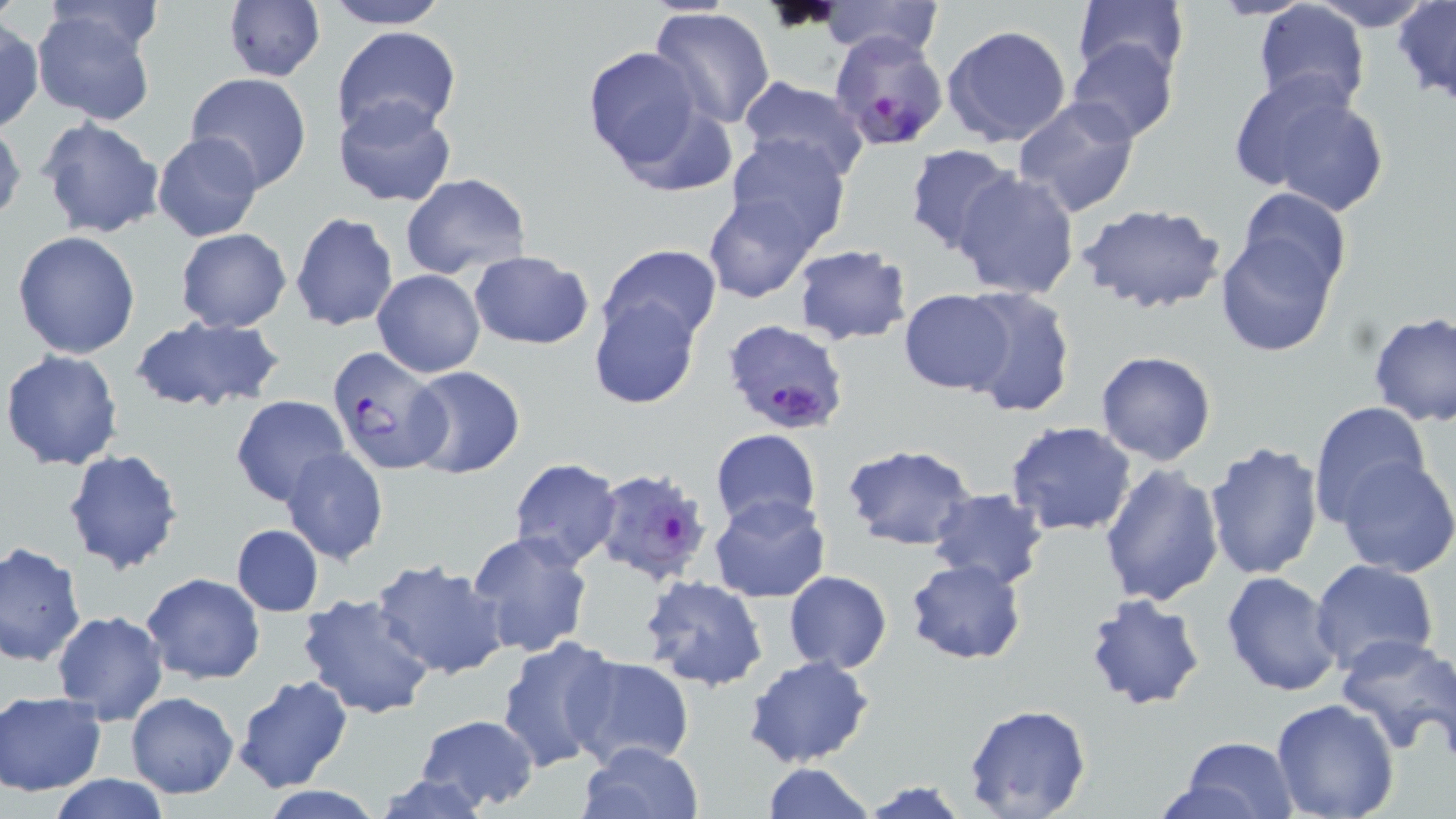
slide-level diagnosis = Plasmodium falciparum
field of view = single
uninfected red blood cell locations = approximate bounding boxes as [x1, y1, x2, y2] in pixels: [318, 0, 453, 28], [820, 0, 945, 62], [1073, 0, 1190, 86], [1310, 0, 1437, 29], [1393, 0, 1456, 107], [223, 2, 324, 83], [1252, 3, 1370, 117], [30, 5, 162, 126], [649, 7, 776, 129], [0, 19, 43, 134], [942, 24, 1073, 149], [331, 26, 461, 139], [1068, 38, 1179, 142], [580, 45, 715, 179], [184, 72, 313, 192], [1231, 73, 1393, 216], [735, 77, 872, 184], [331, 95, 458, 209], [1012, 95, 1141, 215], [36, 116, 164, 240], [0, 119, 25, 227], [152, 134, 264, 241], [723, 135, 849, 251], [903, 145, 1020, 258], [950, 168, 1082, 300], [400, 173, 530, 277], [1236, 186, 1351, 290], [704, 194, 820, 302], [1076, 203, 1227, 315], [289, 211, 400, 333], [175, 228, 292, 332], [11, 230, 142, 360], [1215, 231, 1340, 357], [790, 243, 914, 346], [600, 245, 721, 346], [466, 250, 594, 349], [373, 269, 485, 378], [959, 287, 1077, 417], [899, 289, 1017, 394], [587, 294, 701, 410], [1368, 312, 1456, 426], [127, 316, 287, 414], [2, 349, 124, 471], [1095, 350, 1216, 466], [404, 365, 526, 479], [231, 395, 352, 510], [1306, 400, 1433, 520], [1004, 420, 1138, 537], [710, 428, 821, 531], [1204, 440, 1324, 581], [841, 442, 979, 551], [281, 447, 388, 564], [62, 448, 183, 575], [1334, 456, 1456, 577], [508, 458, 623, 569], [1096, 463, 1224, 610], [927, 488, 1050, 590], [710, 495, 831, 604], [231, 523, 324, 617], [468, 531, 593, 657], [0, 543, 87, 667], [371, 558, 509, 680], [905, 558, 1027, 665], [1309, 560, 1441, 677], [1222, 570, 1345, 698], [783, 571, 892, 672], [141, 572, 267, 684], [640, 575, 770, 690], [298, 592, 438, 721], [1081, 593, 1206, 711], [51, 609, 169, 724], [1334, 632, 1456, 755], [495, 635, 621, 773], [1420, 645, 1455, 766], [563, 654, 695, 773], [743, 655, 876, 769], [233, 673, 353, 794], [1, 691, 105, 796], [125, 691, 240, 798], [1268, 698, 1401, 819], [963, 703, 1093, 819], [414, 712, 541, 811], [1170, 734, 1303, 818], [577, 740, 704, 819], [759, 762, 876, 819], [372, 767, 500, 819], [42, 776, 176, 818], [859, 777, 973, 819]
modality = optical microscopy
magnification = 1000x
stain = May-Grünwald-Giemsa
image size = 1456×819 pixels
Plasmodium falciparum-infected red blood cell locations = approximate bounding boxes as [x1, y1, x2, y2] in pixels: [833, 26, 949, 153], [722, 321, 850, 436], [328, 348, 454, 473], [592, 467, 716, 590]
preparation = thin blood smear